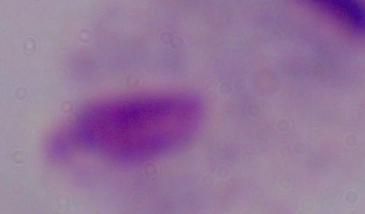
Summary:
  - Modality: photomicrograph
  - Magnification: 1000x
  - Identification: trichomonad